Assess this cell for malaria.
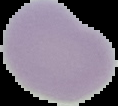

Uninfected.

Summary:
  - Image size: 118×106 pixels
  - Image type: segmented cell region on a black background
  - Preparation: thin blood smear